Report the malaria status of this cell.
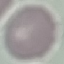
It is uninfected.

Photographed with a smartphone camera at the microscope eyepiece. Cell patch, automatically extracted from a larger field of view and resized to 64 × 64 pixels. Thin smear of blood. Giemsa stain.